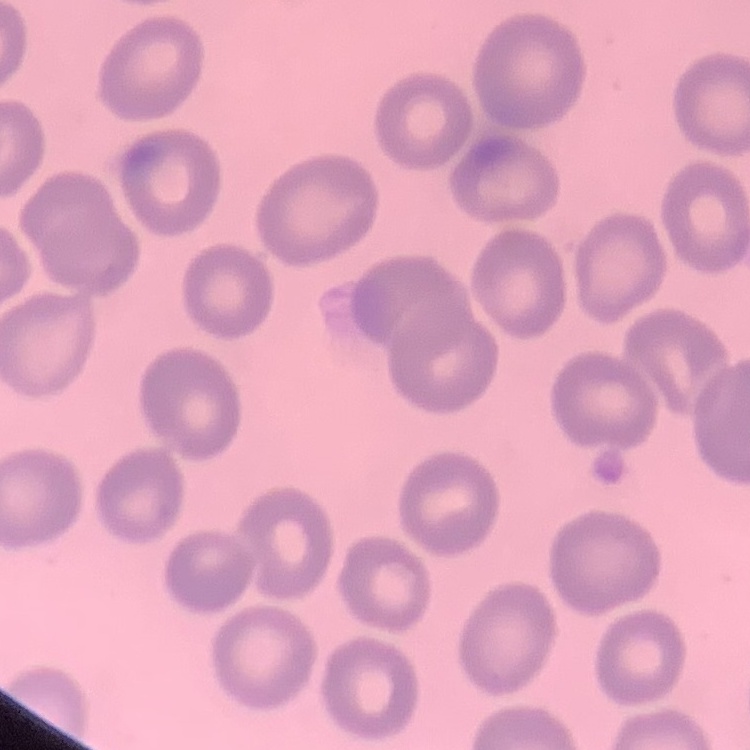
The red blood cells exhibit no rouleaux formation. Stained with either Field's or Giemsa. One tile cut from a larger photomicrograph. Thin peripheral smear.